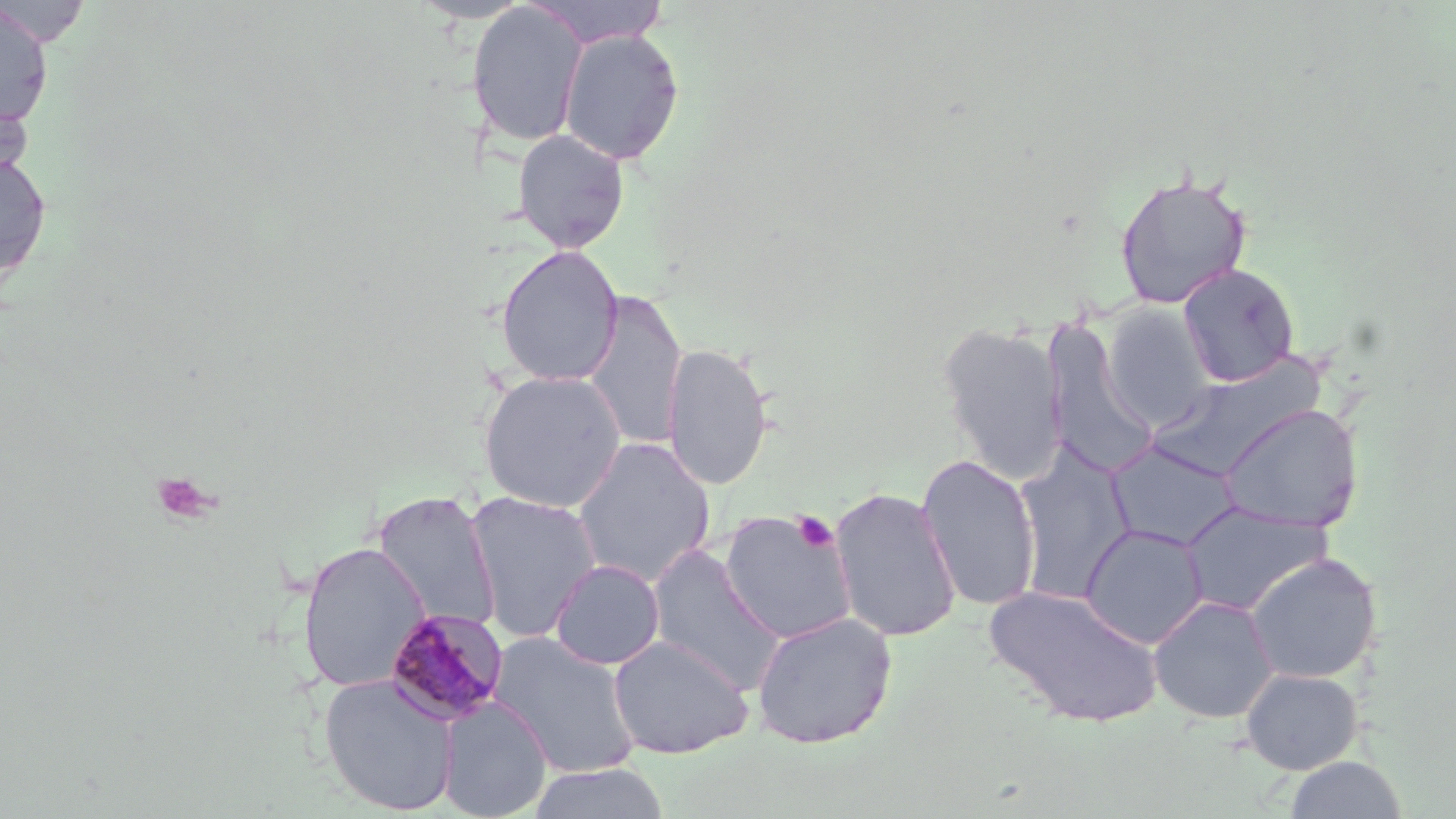

slide-level diagnosis = Plasmodium malariae
stain = May-Grünwald-Giemsa
Plasmodium malariae-infected red blood cell locations = approximate bounding boxes as (x1, y1, x2, y2) in pixels: (383, 608, 510, 727)
preparation = thin blood film
image size = 1456×819 pixels
modality = light microscopy
platelet locations = approximate bounding boxes as (x1, y1, x2, y2) in pixels: (792, 511, 839, 552)
magnification = 1000x
field of view = one of a larger specimen
uninfected red blood cell locations = approximate bounding boxes as (x1, y1, x2, y2) in pixels: (412, 0, 532, 23), (526, 0, 670, 48), (467, 2, 587, 147), (0, 3, 54, 127), (558, 29, 684, 165), (0, 93, 33, 189), (511, 128, 630, 253), (0, 152, 52, 281), (1113, 170, 1253, 310), (495, 245, 624, 387), (1178, 263, 1299, 387), (582, 290, 688, 453), (1101, 303, 1217, 431), (1041, 318, 1156, 479), (937, 321, 1068, 485), (662, 342, 774, 491), (478, 370, 627, 512), (1219, 403, 1363, 533), (571, 437, 715, 588), (1106, 441, 1242, 552), (1013, 448, 1135, 604), (916, 453, 1041, 612), (828, 486, 962, 643), (372, 490, 502, 634), (465, 491, 602, 643), (1180, 503, 1332, 616), (718, 508, 857, 645), (1080, 523, 1209, 649), (297, 541, 429, 693), (645, 544, 787, 696), (1244, 553, 1382, 684), (550, 559, 664, 670), (981, 584, 1164, 728), (1148, 595, 1279, 724), (751, 611, 897, 749), (487, 632, 641, 778), (608, 635, 753, 759), (1240, 667, 1363, 774), (319, 673, 460, 816), (438, 697, 553, 818), (1283, 756, 1409, 818), (526, 762, 672, 819)